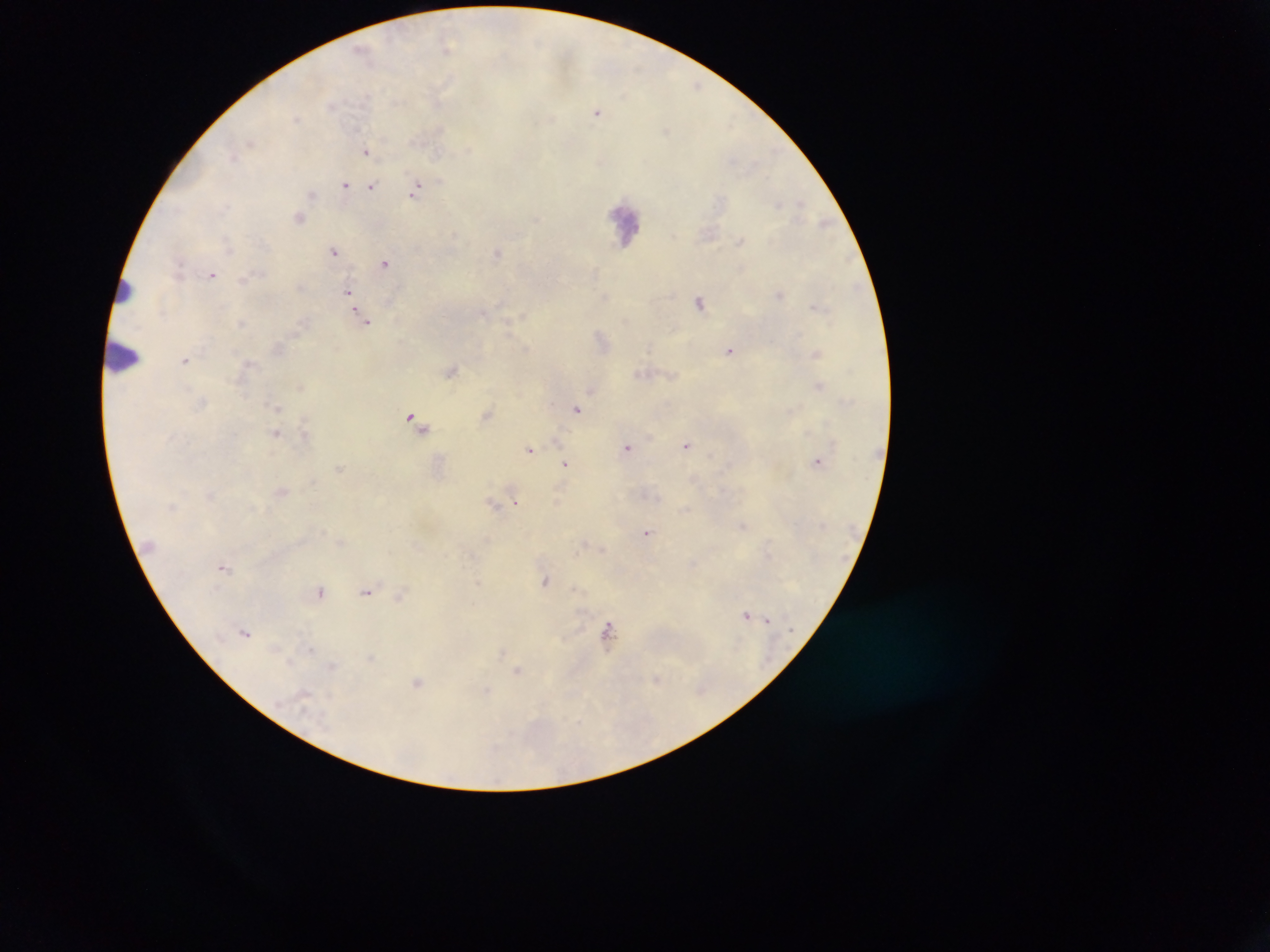

Approximate centers as x y in pixels. Leukocyte locations: 625 222; 124 293; 122 356. Malaria parasite locations: 448 48; 363 50; 598 111; 367 150; 345 185; 372 186; 417 188; 312 194; 300 217; 823 223; 741 240; 334 251; 498 252; 385 263; 212 274; 244 280; 349 293; 780 295; 701 301; 364 318; 243 322; 603 339; 729 350; 817 352; 186 360; 451 370; 642 374; 302 385; 820 385; 593 390; 278 407; 577 408; 487 413; 412 419; 424 425; 276 432; 306 434; 688 445; 628 447; 530 449; 818 460; 567 464; 339 468; 281 491; 558 500; 493 503; 515 503; 685 509; 743 525; 648 533; 583 545; 602 548; 225 566; 546 581; 321 591; 367 591; 401 597; 747 615; 767 620; 246 631; 609 631; 370 658; 518 670; 656 679; 418 681. Collected in Ghana. Image is 1270×952 pixels. Thick blood smear. Photographed through a microscope with a mobile-phone camera. Single field of view.